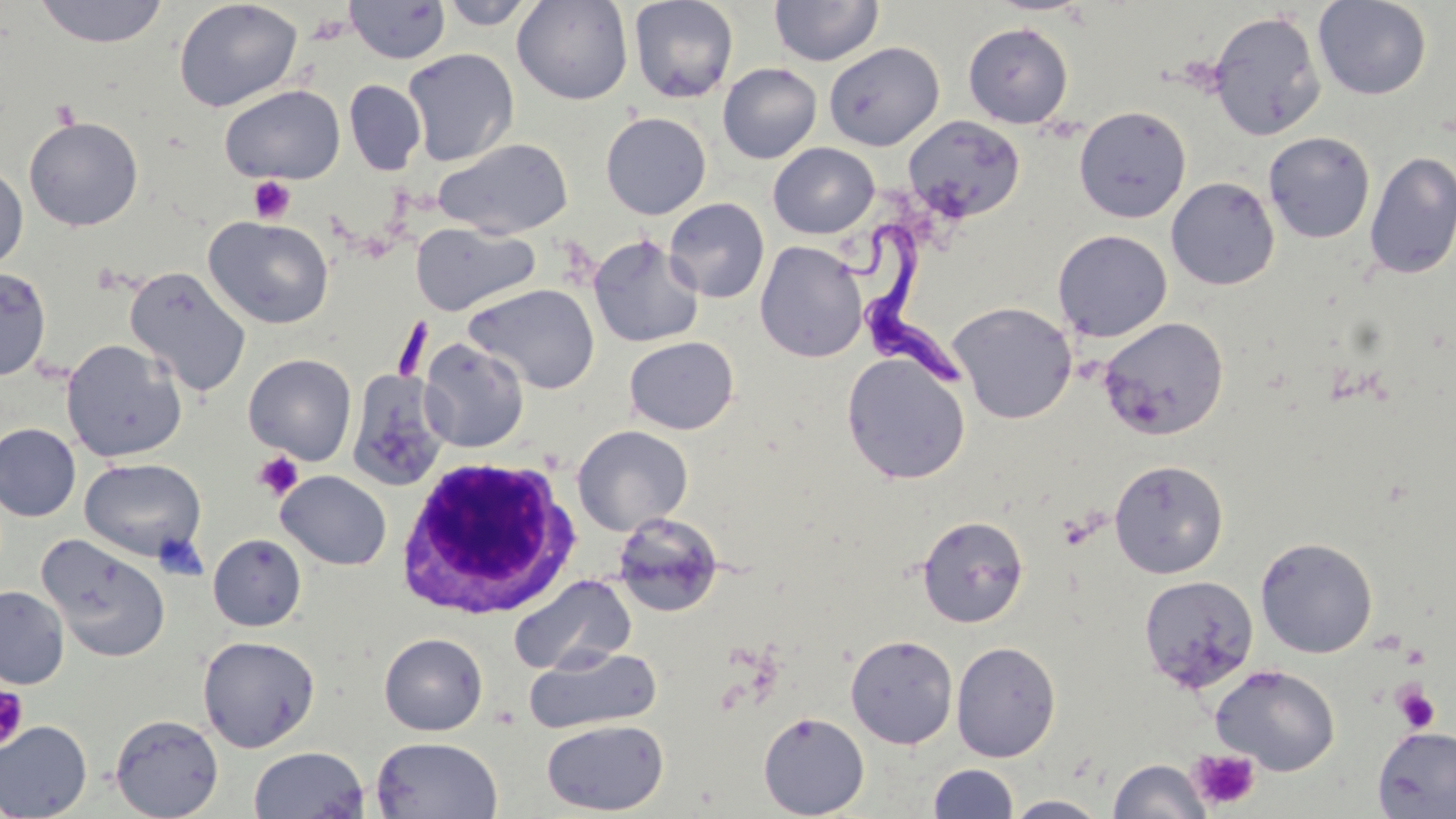
Summary:
  - Coordinate format: approximate bounding boxes as (x1,y1)-(x2,y2) corner pairs in pixels
  - Platelet locations: (248,176)-(295,223), (254,452)-(303,499), (1392,683)-(1441,734), (0,686)-(28,750), (1188,749)-(1260,811)
  - White blood cell locations: (394,455)-(580,620)
  - Uninfected red blood cell locations: (34,0)-(169,48), (174,0)-(302,113), (438,0)-(540,29), (511,0)-(634,105), (628,0)-(739,104), (1312,0)-(1432,100), (345,1)-(450,64), (769,1)-(884,67), (1208,10)-(1326,141), (963,22)-(1073,128), (823,42)-(945,150), (402,48)-(519,166), (717,63)-(822,164), (344,80)-(426,175), (220,85)-(345,184), (1074,105)-(1192,223), (600,112)-(711,219), (24,116)-(143,231), (903,116)-(1025,223), (1263,131)-(1376,243), (434,137)-(573,238), (768,142)-(879,238), (1364,150)-(1456,280), (0,164)-(28,272), (1165,176)-(1280,290), (664,198)-(770,303), (205,216)-(334,329), (410,222)-(539,316), (1053,229)-(1173,342), (588,234)-(704,348), (755,241)-(868,362), (0,266)-(52,381), (124,266)-(251,397), (464,283)-(601,394), (948,301)-(1078,424), (1098,316)-(1229,440), (624,336)-(739,435), (418,338)-(529,453), (61,339)-(187,462), (841,352)-(971,485), (244,353)-(357,465), (346,370)-(450,490), (0,423)-(81,522), (572,425)-(693,536), (79,457)-(206,562), (1109,459)-(1229,579), (277,470)-(392,570), (611,512)-(723,618), (917,515)-(1029,628), (37,533)-(171,662), (208,534)-(307,631), (1254,536)-(1379,658), (1138,574)-(1259,693), (507,575)-(638,675), (0,585)-(70,690), (379,632)-(487,736), (845,634)-(958,748), (198,635)-(320,752), (951,641)-(1061,761), (524,646)-(662,734), (1211,664)-(1341,775), (758,711)-(870,818), (109,714)-(224,818), (541,719)-(669,815), (0,720)-(93,819), (1372,726)-(1456,818), (370,736)-(503,819), (249,746)-(370,819), (1108,758)-(1211,819), (928,763)-(1019,819), (1004,794)-(1109,818)
  - Trypanosoma brucei locations: (841,216)-(973,392)
  - Slide-level diagnosis: Trypanosoma brucei
  - Stain: May-Grünwald-Giemsa
  - Modality: optical microscopy
  - Field of view: single
  - Preparation: thin blood smear
  - Magnification: 1000x
  - Image size: 1456×819 pixels